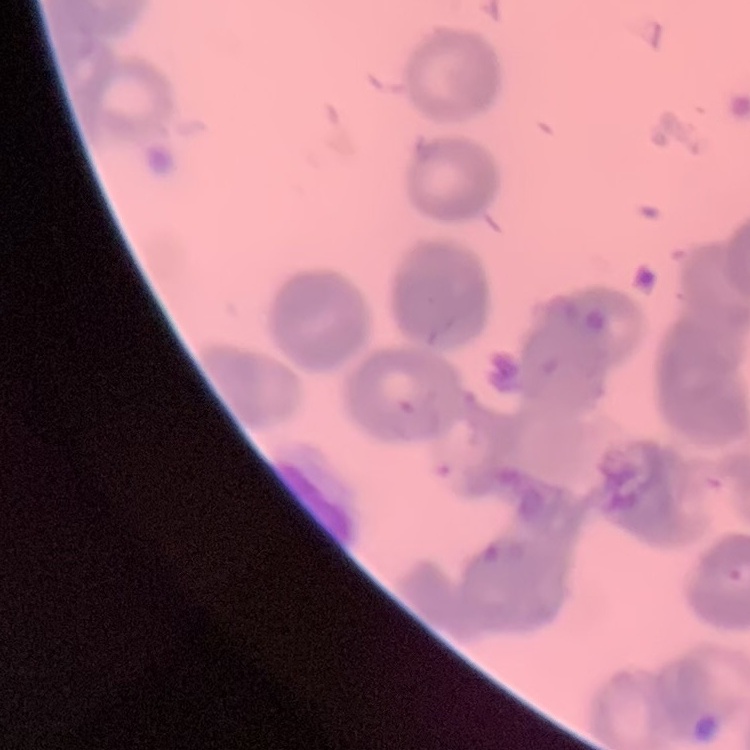
The erythrocytes exhibit rouleaux formation. Stained with either Field's or Giemsa. Thin blood smear. Square crop of a larger photomicrograph.